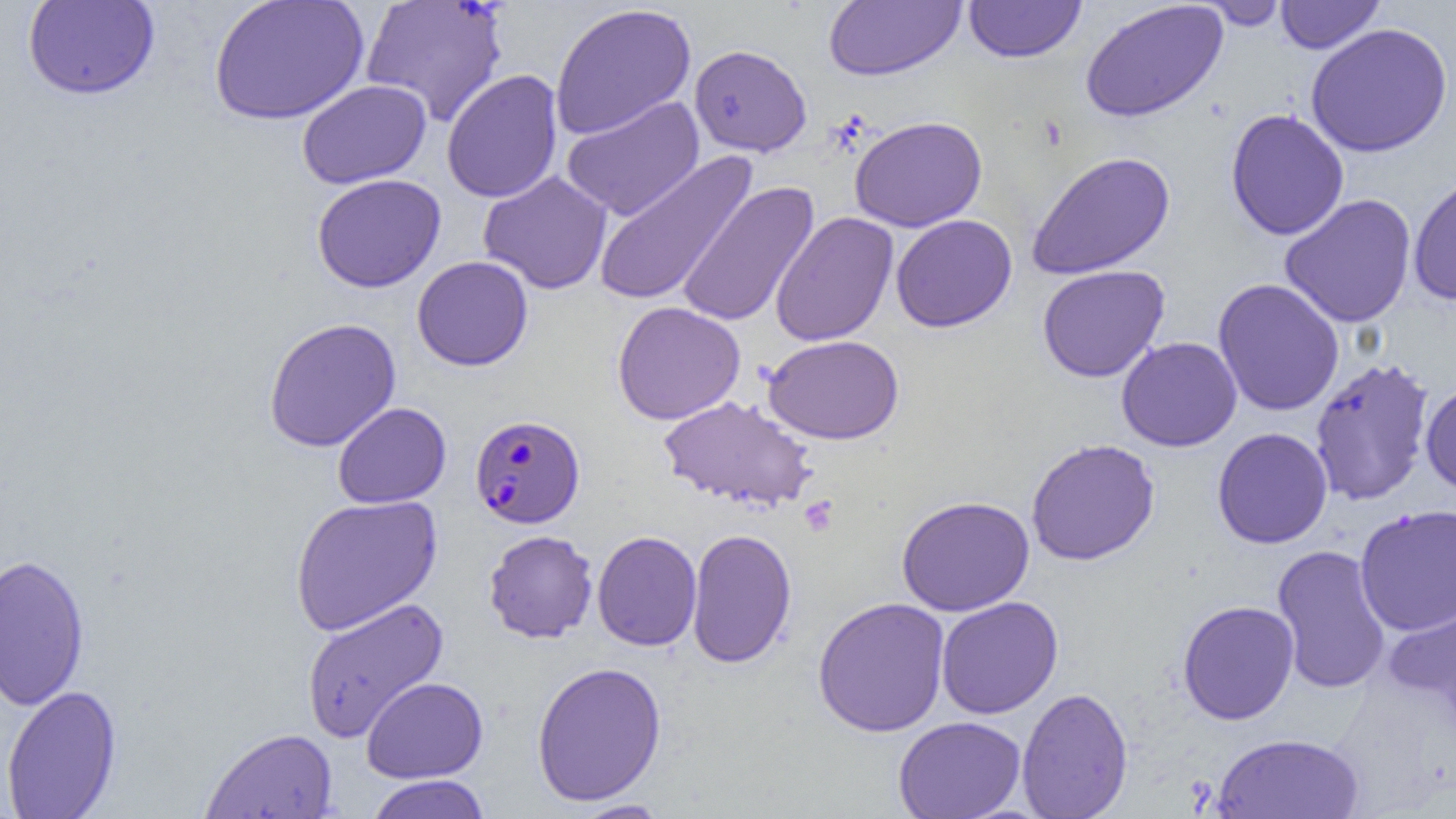

Approximate bounding boxes as named x1/y1/x2/y2 corners in pixels. Plasmodium falciparum-infected red blood cell locations: (x1=469, y1=414, x2=585, y2=528). Uninfected red blood cell locations: (x1=22, y1=0, x2=160, y2=100), (x1=208, y1=0, x2=369, y2=125), (x1=362, y1=0, x2=509, y2=127), (x1=963, y1=0, x2=1087, y2=63), (x1=1275, y1=0, x2=1385, y2=53), (x1=823, y1=1, x2=967, y2=81), (x1=1198, y1=1, x2=1290, y2=30), (x1=1080, y1=2, x2=1229, y2=123), (x1=549, y1=3, x2=696, y2=139), (x1=1305, y1=22, x2=1453, y2=157), (x1=689, y1=44, x2=812, y2=157), (x1=441, y1=70, x2=562, y2=203), (x1=297, y1=80, x2=431, y2=189), (x1=561, y1=96, x2=705, y2=222), (x1=1225, y1=108, x2=1350, y2=241), (x1=850, y1=115, x2=987, y2=232), (x1=1026, y1=150, x2=1176, y2=279), (x1=593, y1=153, x2=756, y2=306), (x1=478, y1=170, x2=613, y2=294), (x1=1407, y1=172, x2=1456, y2=306), (x1=312, y1=174, x2=446, y2=293), (x1=676, y1=180, x2=820, y2=328), (x1=1279, y1=194, x2=1417, y2=329), (x1=770, y1=212, x2=898, y2=346), (x1=890, y1=214, x2=1018, y2=333), (x1=412, y1=255, x2=533, y2=371), (x1=1037, y1=265, x2=1170, y2=382), (x1=1212, y1=278, x2=1345, y2=417), (x1=611, y1=301, x2=746, y2=425), (x1=263, y1=317, x2=401, y2=452), (x1=763, y1=334, x2=904, y2=444), (x1=1116, y1=336, x2=1242, y2=452), (x1=1309, y1=357, x2=1436, y2=506), (x1=1420, y1=379, x2=1456, y2=497), (x1=658, y1=395, x2=819, y2=513), (x1=332, y1=402, x2=451, y2=508), (x1=1212, y1=427, x2=1333, y2=549), (x1=1025, y1=438, x2=1160, y2=565), (x1=289, y1=494, x2=443, y2=636), (x1=896, y1=495, x2=1035, y2=615), (x1=1355, y1=504, x2=1456, y2=635), (x1=686, y1=528, x2=797, y2=669), (x1=484, y1=529, x2=598, y2=643), (x1=592, y1=530, x2=702, y2=651), (x1=1271, y1=545, x2=1392, y2=695), (x1=0, y1=553, x2=91, y2=712), (x1=1382, y1=590, x2=1456, y2=725), (x1=301, y1=596, x2=450, y2=743), (x1=812, y1=596, x2=951, y2=737), (x1=936, y1=596, x2=1063, y2=719), (x1=1177, y1=600, x2=1300, y2=725), (x1=531, y1=661, x2=667, y2=806), (x1=361, y1=676, x2=488, y2=783), (x1=1, y1=684, x2=123, y2=819), (x1=1017, y1=687, x2=1133, y2=819), (x1=893, y1=716, x2=1026, y2=819), (x1=200, y1=727, x2=339, y2=818), (x1=1212, y1=732, x2=1364, y2=818), (x1=365, y1=774, x2=492, y2=819), (x1=568, y1=799, x2=672, y2=818). Platelet locations: (x1=799, y1=496, x2=839, y2=537). Slide-level diagnosis: Plasmodium falciparum. Optical microscopy. 1000x magnification. Image is 1456×819 pixels. Thin blood smear. One field of a larger specimen.